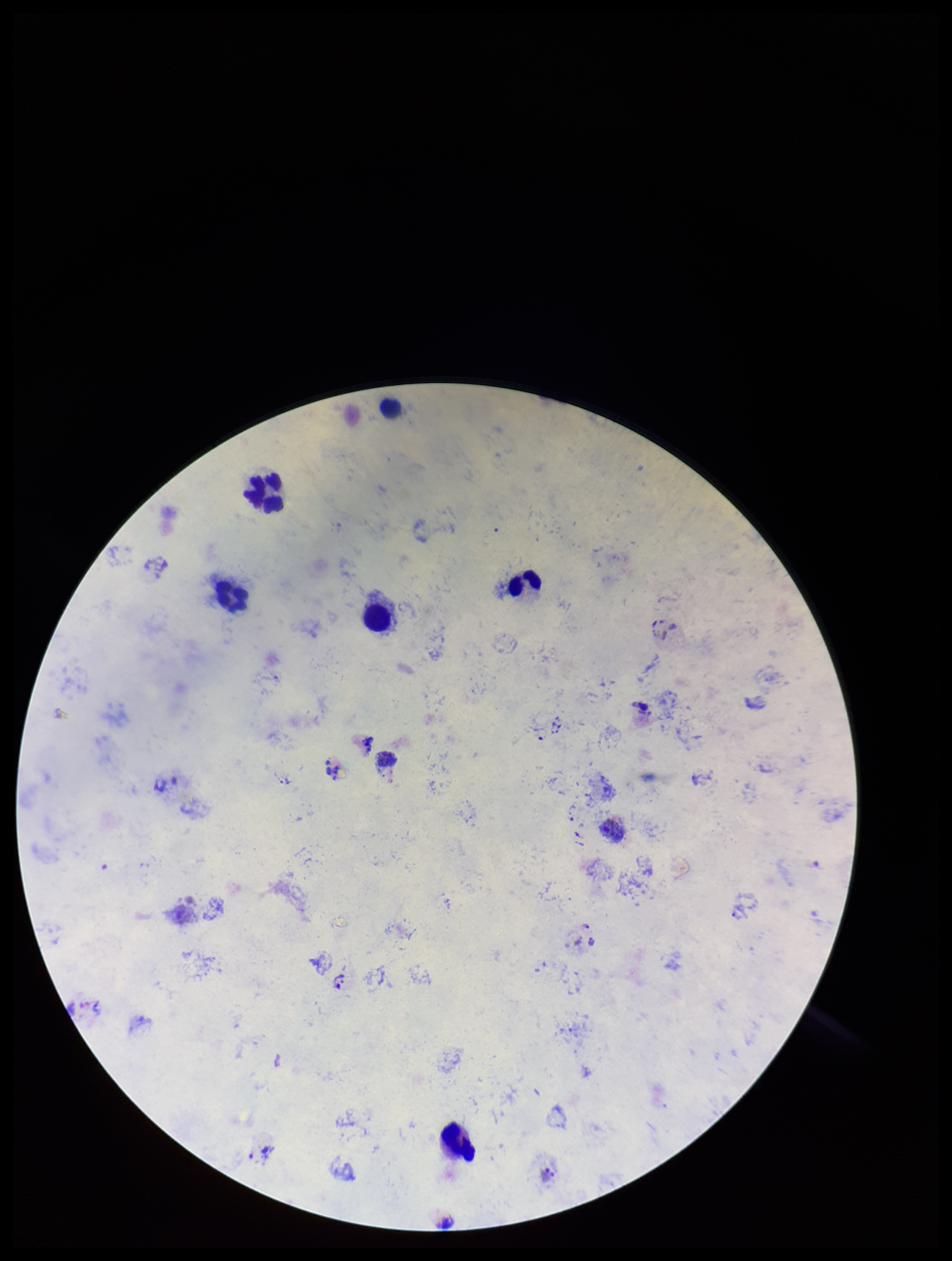
Leukocyte count: 6. Single field of view. Smartphone photograph taken through the eyepiece of a microscope. Species reported for this patient: Plasmodium vivax. Patient malaria status: infected. Image is 952×1261 pixels. Plasmodium parasites: identified. Parasite count: 2. Preparation: thick. Stained with Giemsa.